Locate Plasmodium parasites and leukocytes.
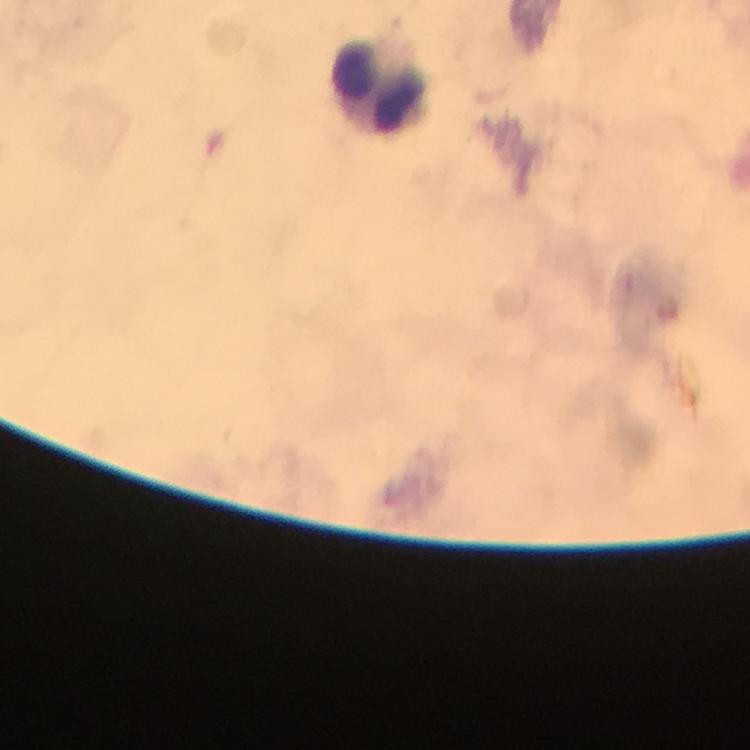

No Plasmodium parasites detected.
Approximate centers as (x, y) in pixels.
Leukocytes: (376, 79).

capture: smartphone camera through the microscope
preparation: thick blood smear
immersion_oil: applied
context: from a malaria diagnostic workup
magnification: 100x
image_size: 750×750 pixels
stain: Giemsa
cropped_from: one field of view